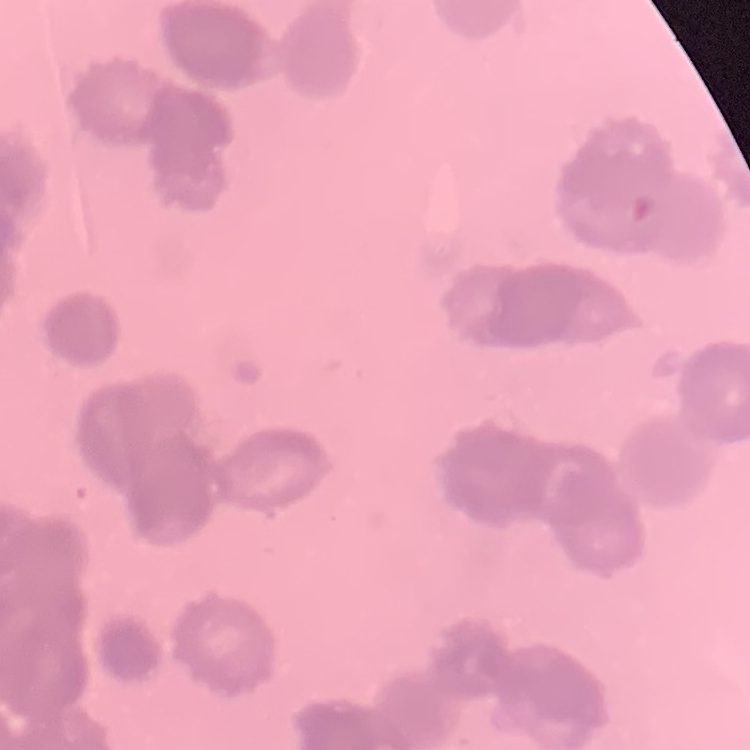
The erythrocytes exhibit rouleaux formation. Square crop of a larger photomicrograph. Stained with either Field's or Giemsa. Thin peripheral smear.